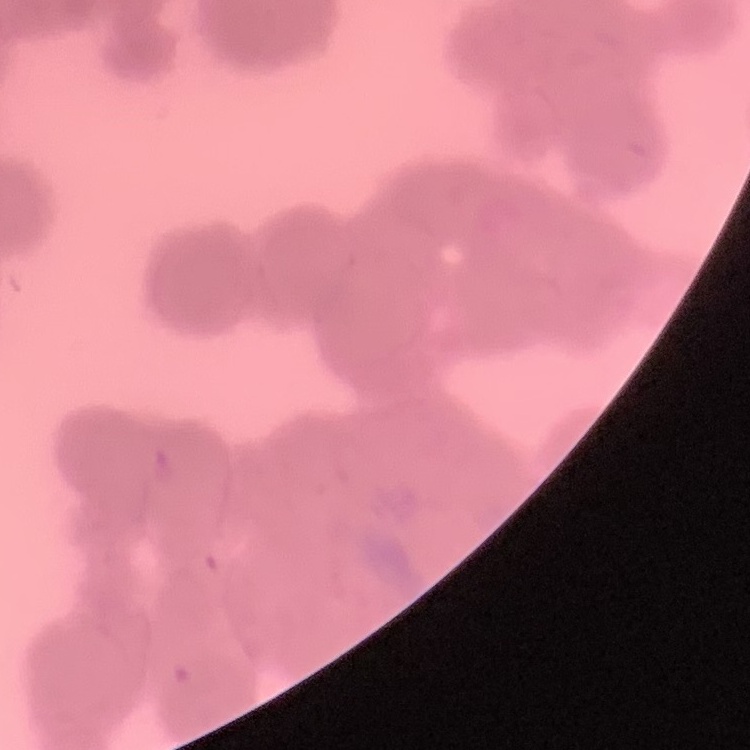
Summary:
  - Erythrocyte morphology: rouleaux formation
  - Image type: one tile cut from a larger photomicrograph
  - Stain: Field's or Giemsa
  - Preparation: thin blood smear